Classify this cell by malaria status.
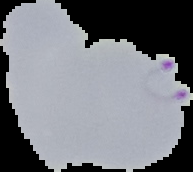
It is parasitized.

Summary:
  - Preparation: thin blood smear
  - Image type: segmented cell region on a black background
  - Image size: 193×172 pixels